Report the malaria status of this cell.
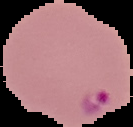
Parasitized.

Image is 133×127 pixels. From a thin blood film. The area outside the segmented cell region is set to black.